Report the malaria status of this cell.
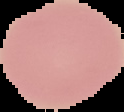
Uninfected.

Image is 124×112 pixels. The area outside the segmented cell region is set to black. From a thin blood film.